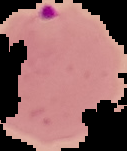
Result: malaria parasites identified. Segmented cell region on a black background. Image is 127×151 pixels. From a thin blood smear.